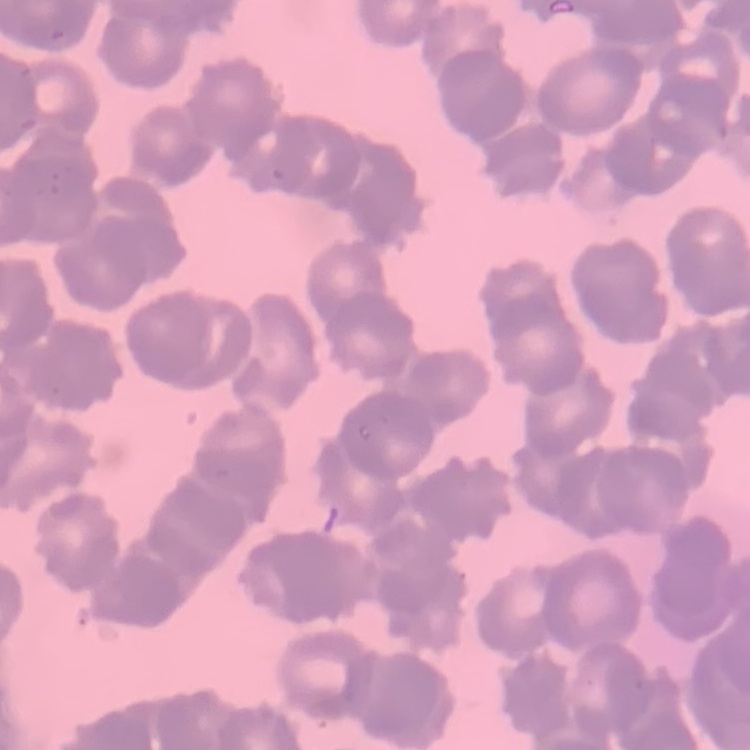
{
  "red_blood_cell_morphology": "rouleaux formation",
  "preparation": "thin blood smear",
  "stain": "Field's or Giemsa",
  "image_type": "one tile cut from a larger photomicrograph"
}